Assess the morphology of the erythrocytes.
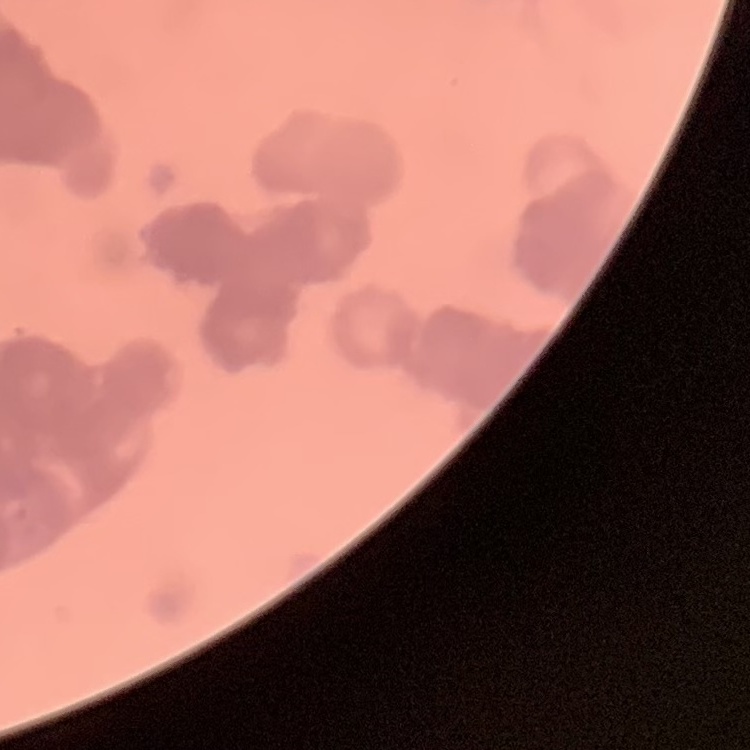

They show rouleaux formation.

image type = square crop of a larger photomicrograph
preparation = thin blood smear
stain = Field's or Giemsa